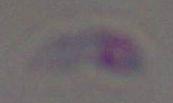
Toxoplasma gondii is seen. Captured at 1000x magnification. Photomicrograph.